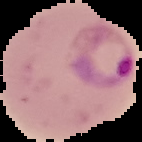
Summary:
  - Image type: cell region segmented out of the field of view; surrounding area masked to black
  - Preparation: thin blood film
  - Result: Plasmodium parasites detected
  - Image size: 142×142 pixels